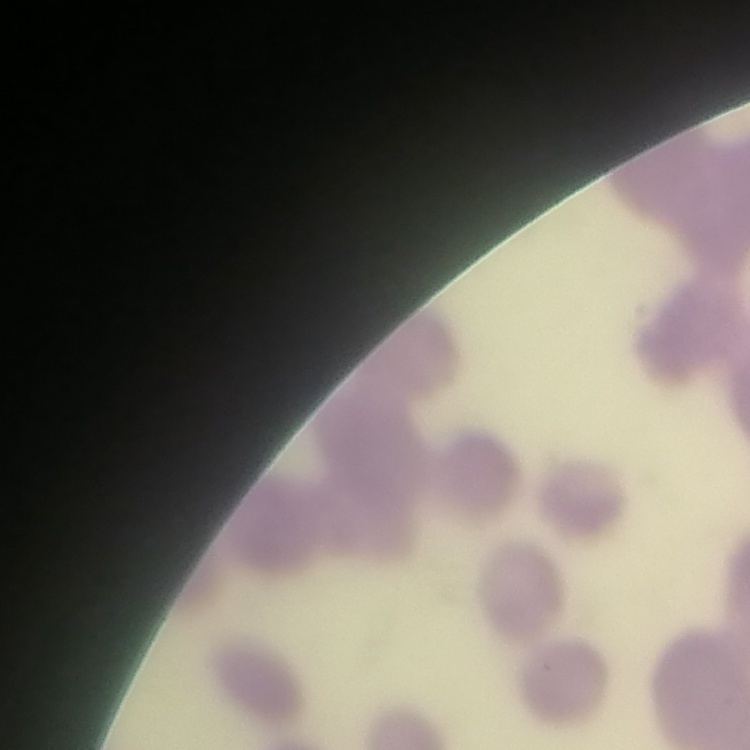 The red blood cells show rouleaux formation. Thin blood smear. Square crop of a larger photomicrograph. Field's or Giemsa stain.